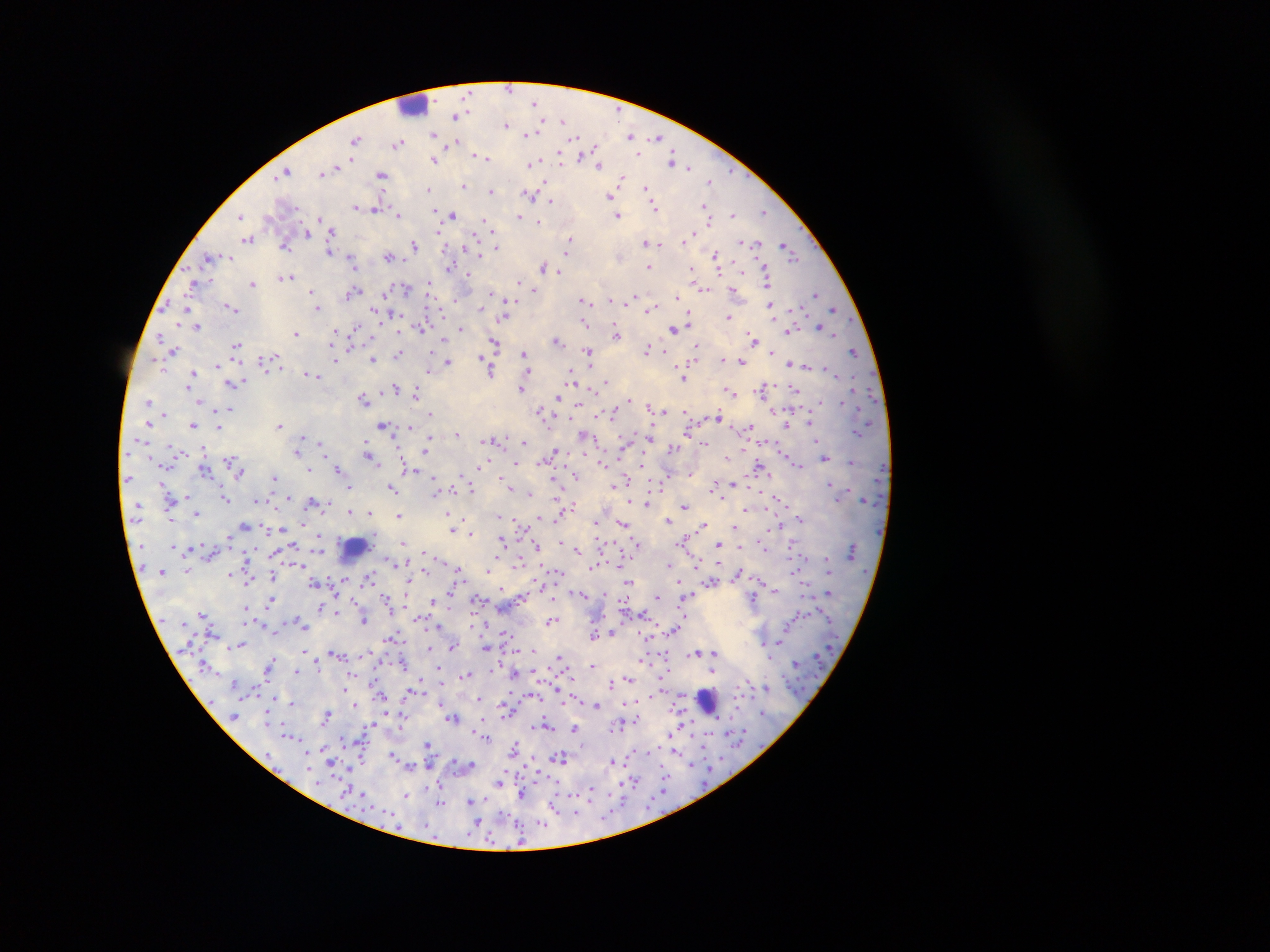

Approximate centers as {x, y} in pixels.
Summary:
  - Malaria parasite locations: {509, 89}, {535, 103}, {455, 115}, {563, 120}, {541, 123}, {506, 125}, {527, 134}, {433, 135}, {631, 136}, {575, 138}, {658, 138}, {356, 139}, {399, 143}, {450, 143}, {596, 148}, {638, 153}, {475, 155}, {479, 156}, {580, 156}, {485, 158}, {352, 159}, {560, 159}, {433, 160}, {673, 160}, {532, 163}, {598, 165}, {689, 167}, {334, 168}, {286, 171}, {322, 172}, {281, 175}, {382, 175}, {621, 179}, {709, 181}, {545, 183}, {463, 186}, {429, 188}, {646, 188}, {490, 192}, {530, 195}, {610, 196}, {550, 202}, {704, 206}, {356, 207}, {654, 207}, {377, 208}, {434, 209}, {763, 212}, {398, 215}, {453, 215}, {733, 215}, {519, 216}, {618, 216}, {240, 217}, {319, 219}, {538, 221}, {486, 222}, {492, 230}, {332, 232}, {440, 232}, {306, 233}, {474, 234}, {442, 236}, {687, 238}, {248, 239}, {570, 239}, {743, 242}, {646, 243}, {757, 243}, {658, 244}, {785, 244}, {414, 245}, {285, 246}, {495, 247}, {329, 251}, {791, 253}, {715, 254}, {479, 255}, {388, 256}, {210, 257}, {794, 258}, {350, 261}, {543, 265}, {449, 268}, {649, 268}, {692, 269}, {718, 270}, {558, 272}, {468, 275}, {287, 277}, {520, 281}, {767, 281}, {192, 283}, {253, 283}, {430, 284}, {407, 288}, {703, 289}, {534, 290}, {311, 291}, {733, 291}, {491, 293}, {353, 294}, {816, 294}, {636, 296}, {676, 297}, {583, 300}, {610, 300}, {628, 301}, {771, 307}, {189, 308}, {231, 308}, {317, 308}, {480, 308}, {834, 309}, {374, 310}, {650, 310}, {394, 314}, {688, 314}, {728, 316}, {505, 317}, {585, 325}, {197, 327}, {357, 327}, {461, 327}, {420, 328}, {821, 328}, {674, 330}, {336, 331}, {790, 332}, {296, 334}, {616, 334}, {834, 334}, {160, 336}, {752, 336}, {444, 338}, {556, 340}, {494, 342}, {236, 345}, {696, 346}, {648, 349}, {174, 350}, {588, 352}, {772, 352}, {524, 353}, {665, 353}, {855, 353}, {398, 355}, {695, 356}, {482, 357}, {723, 358}, {336, 359}, {372, 359}, {447, 361}, {742, 362}, {790, 364}, {217, 365}, {428, 369}, {491, 371}, {191, 375}, {315, 376}, {570, 376}, {684, 378}, {190, 379}, {240, 382}, {605, 382}, {235, 383}, {188, 384}, {521, 388}, {762, 388}, {395, 389}, {795, 390}, {729, 392}, {415, 394}, {364, 397}, {558, 397}, {629, 399}, {149, 400}, {820, 401}, {201, 403}, {577, 404}, {231, 408}, {540, 410}, {661, 410}, {685, 412}, {612, 413}, {431, 414}, {164, 415}, {719, 415}, {811, 422}, {383, 424}, {787, 424}, {193, 425}, {279, 425}, {410, 427}, {750, 427}, {219, 428}, {458, 433}, {586, 436}, {650, 436}, {429, 439}, {300, 440}, {523, 441}, {321, 443}, {705, 443}, {427, 444}, {366, 446}, {672, 447}, {427, 448}, {297, 451}, {554, 452}, {368, 453}, {371, 457}, {825, 457}, {852, 463}, {482, 464}, {516, 464}, {642, 464}, {799, 464}, {339, 468}, {761, 468}, {309, 470}, {239, 473}, {574, 476}, {274, 477}, {625, 480}, {665, 480}, {732, 483}, {507, 485}, {613, 485}, {349, 486}, {714, 486}, {391, 488}, {472, 488}, {437, 491}, {452, 491}, {529, 493}, {556, 494}, {186, 496}, {288, 497}, {226, 499}, {779, 500}, {258, 501}, {312, 501}, {630, 503}, {647, 504}, {572, 505}, {685, 506}, {744, 511}, {350, 512}, {369, 512}, {197, 514}, {448, 514}, {399, 516}, {800, 519}, {462, 520}, {668, 520}, {597, 522}, {622, 524}, {245, 526}, {703, 526}, {735, 526}, {283, 529}, {453, 529}, {471, 533}, {319, 536}, {502, 540}, {403, 543}, {637, 543}, {718, 544}, {293, 545}, {793, 545}, {537, 547}, {578, 550}, {425, 552}, {519, 562}, {490, 566}, {669, 566}, {592, 567}, {458, 568}, {488, 571}, {557, 571}, {739, 573}, {230, 574}, {272, 576}, {370, 578}, {315, 582}, {627, 582}, {712, 582}, {582, 594}, {687, 596}, {386, 597}, {657, 597}, {753, 598}, {476, 599}, {553, 599}, {271, 601}, {432, 601}, {320, 607}, {246, 608}, {337, 613}, {203, 615}, {420, 618}, {363, 620}, {552, 620}, {303, 624}, {440, 625}, {673, 629}, {505, 632}, {611, 632}, {594, 635}, {393, 637}, {239, 646}, {429, 647}, {452, 647}, {486, 647}, {695, 653}, {715, 655}, {559, 657}, {270, 663}, {594, 666}, {298, 670}, {440, 670}, {713, 671}, {466, 675}, {629, 678}, {611, 684}, {344, 688}, {479, 699}, {292, 703}, {596, 704}, {354, 705}, {325, 715}, {453, 718}, {636, 719}, {546, 725}, {575, 728}, {291, 736}, {428, 744}, {514, 748}, {393, 755}, {561, 758}, {612, 761}, {411, 765}, {472, 765}, {499, 781}, {632, 783}, {590, 792}, {522, 793}, {406, 796}, {471, 801}, {440, 802}, {553, 808}, {503, 814}, {544, 822}, {477, 823}, {519, 839}
  - Leukocyte locations: {414, 107}, {355, 549}, {705, 703}
  - Capture: mobile-phone photograph through a microscope
  - Preparation: thick blood smear
  - Country: Ghana
  - Field of view: single
  - Image size: 1270×952 pixels